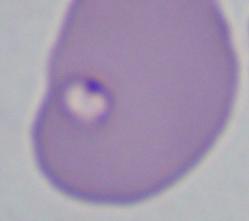

Summary:
  - Identification: Babesia
  - Magnification: 1000x
  - Modality: micrograph